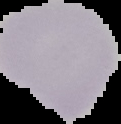

Summary:
  - Malaria status: uninfected
  - Preparation: thin blood smear
  - Image size: 121×124 pixels
  - Image type: segmented cell region on a black background